Locate every uninfected red blood cell.
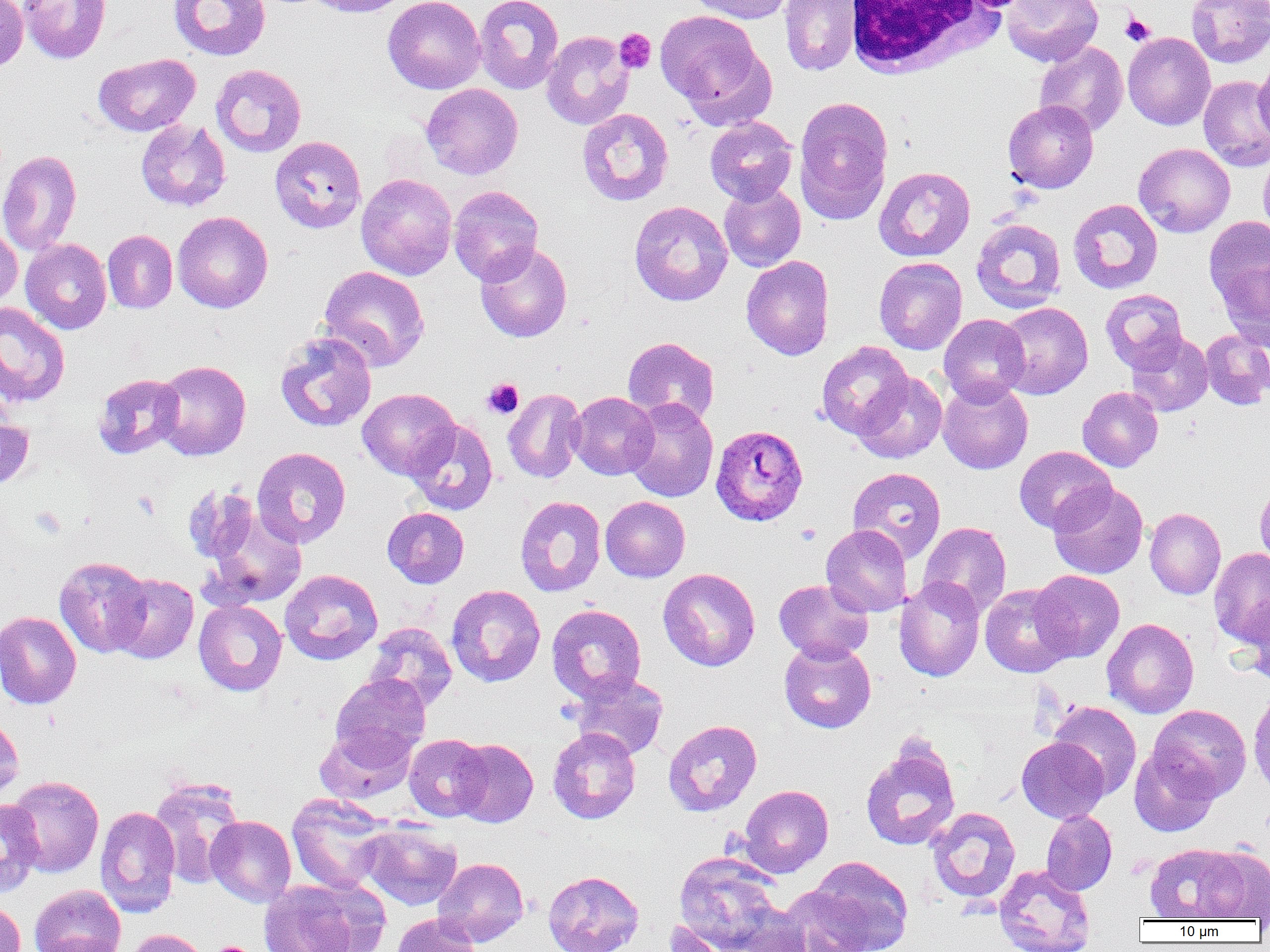
Approximate bounding boxes as named x1/y1/x2/y2 corners in pixels.
Uninfected red blood cells: (x1=0, y1=0, x2=28, y2=73), (x1=20, y1=0, x2=111, y2=64), (x1=168, y1=0, x2=270, y2=60), (x1=304, y1=0, x2=414, y2=17), (x1=383, y1=0, x2=485, y2=94), (x1=474, y1=0, x2=564, y2=94), (x1=685, y1=0, x2=794, y2=24), (x1=1002, y1=0, x2=1103, y2=67), (x1=1186, y1=0, x2=1270, y2=68), (x1=779, y1=1, x2=860, y2=76), (x1=654, y1=9, x2=769, y2=117), (x1=541, y1=31, x2=634, y2=129), (x1=1123, y1=32, x2=1215, y2=130), (x1=1034, y1=42, x2=1128, y2=136), (x1=93, y1=54, x2=201, y2=136), (x1=1254, y1=57, x2=1270, y2=142), (x1=210, y1=64, x2=307, y2=157), (x1=1199, y1=76, x2=1270, y2=172), (x1=420, y1=83, x2=523, y2=179), (x1=793, y1=96, x2=894, y2=225), (x1=1002, y1=100, x2=1099, y2=194), (x1=577, y1=108, x2=674, y2=206), (x1=705, y1=116, x2=798, y2=205), (x1=136, y1=119, x2=231, y2=211), (x1=269, y1=136, x2=366, y2=234), (x1=1134, y1=143, x2=1235, y2=237), (x1=0, y1=149, x2=82, y2=257), (x1=1258, y1=150, x2=1270, y2=242), (x1=874, y1=167, x2=975, y2=261), (x1=356, y1=173, x2=457, y2=280), (x1=719, y1=181, x2=806, y2=272), (x1=448, y1=185, x2=543, y2=284), (x1=1068, y1=199, x2=1163, y2=293), (x1=629, y1=200, x2=733, y2=306), (x1=172, y1=211, x2=273, y2=313), (x1=1204, y1=215, x2=1270, y2=309), (x1=971, y1=218, x2=1066, y2=313), (x1=0, y1=222, x2=22, y2=309), (x1=102, y1=230, x2=177, y2=313), (x1=21, y1=238, x2=111, y2=334), (x1=474, y1=242, x2=572, y2=342), (x1=741, y1=255, x2=834, y2=361), (x1=874, y1=257, x2=967, y2=355), (x1=1218, y1=258, x2=1270, y2=348), (x1=319, y1=265, x2=430, y2=371), (x1=1100, y1=289, x2=1188, y2=373), (x1=996, y1=301, x2=1093, y2=398), (x1=0, y1=302, x2=70, y2=407), (x1=939, y1=314, x2=1030, y2=406), (x1=1201, y1=328, x2=1270, y2=410), (x1=274, y1=330, x2=377, y2=432), (x1=1126, y1=331, x2=1213, y2=416), (x1=622, y1=336, x2=719, y2=426), (x1=816, y1=341, x2=913, y2=439), (x1=154, y1=360, x2=251, y2=460), (x1=853, y1=371, x2=947, y2=463), (x1=92, y1=373, x2=184, y2=459), (x1=938, y1=379, x2=1033, y2=474), (x1=1077, y1=386, x2=1163, y2=472), (x1=357, y1=388, x2=459, y2=480), (x1=503, y1=388, x2=586, y2=483), (x1=568, y1=392, x2=658, y2=480), (x1=623, y1=397, x2=718, y2=502), (x1=0, y1=414, x2=34, y2=489), (x1=405, y1=419, x2=498, y2=515), (x1=1014, y1=446, x2=1115, y2=534), (x1=252, y1=447, x2=351, y2=548), (x1=847, y1=467, x2=946, y2=563), (x1=1255, y1=481, x2=1270, y2=571), (x1=1048, y1=483, x2=1148, y2=579), (x1=182, y1=484, x2=259, y2=565), (x1=515, y1=495, x2=606, y2=597), (x1=600, y1=496, x2=690, y2=582), (x1=382, y1=507, x2=469, y2=588), (x1=1145, y1=508, x2=1226, y2=599), (x1=205, y1=510, x2=307, y2=609), (x1=919, y1=521, x2=1011, y2=618), (x1=821, y1=524, x2=912, y2=617), (x1=1209, y1=547, x2=1270, y2=647), (x1=54, y1=556, x2=152, y2=657), (x1=658, y1=568, x2=760, y2=671), (x1=280, y1=569, x2=383, y2=665), (x1=1030, y1=570, x2=1124, y2=662), (x1=110, y1=573, x2=199, y2=664), (x1=894, y1=577, x2=985, y2=681), (x1=774, y1=579, x2=873, y2=663), (x1=980, y1=584, x2=1074, y2=678), (x1=446, y1=585, x2=546, y2=687), (x1=1240, y1=594, x2=1269, y2=684), (x1=194, y1=600, x2=287, y2=696), (x1=546, y1=604, x2=646, y2=703), (x1=0, y1=611, x2=81, y2=709), (x1=1102, y1=618, x2=1199, y2=718), (x1=365, y1=622, x2=457, y2=711), (x1=779, y1=639, x2=876, y2=734), (x1=569, y1=672, x2=669, y2=760), (x1=330, y1=673, x2=430, y2=765), (x1=1249, y1=688, x2=1270, y2=797), (x1=1048, y1=701, x2=1142, y2=799), (x1=1148, y1=704, x2=1252, y2=801), (x1=0, y1=715, x2=24, y2=804), (x1=663, y1=719, x2=762, y2=816), (x1=314, y1=726, x2=415, y2=804), (x1=548, y1=727, x2=641, y2=824), (x1=404, y1=734, x2=490, y2=821), (x1=1016, y1=736, x2=1109, y2=823), (x1=450, y1=738, x2=538, y2=828), (x1=860, y1=741, x2=961, y2=850), (x1=1129, y1=745, x2=1219, y2=837), (x1=6, y1=776, x2=104, y2=877), (x1=148, y1=777, x2=246, y2=888), (x1=739, y1=784, x2=833, y2=877), (x1=287, y1=794, x2=393, y2=893), (x1=0, y1=799, x2=43, y2=897), (x1=95, y1=806, x2=181, y2=917), (x1=927, y1=807, x2=1020, y2=903), (x1=1041, y1=809, x2=1117, y2=895), (x1=206, y1=815, x2=296, y2=907), (x1=359, y1=821, x2=462, y2=911), (x1=1145, y1=843, x2=1243, y2=921), (x1=1194, y1=846, x2=1270, y2=920), (x1=674, y1=852, x2=783, y2=951), (x1=805, y1=856, x2=914, y2=951), (x1=433, y1=857, x2=529, y2=947), (x1=994, y1=864, x2=1096, y2=951), (x1=543, y1=870, x2=644, y2=952), (x1=258, y1=879, x2=373, y2=952), (x1=28, y1=884, x2=126, y2=952), (x1=776, y1=884, x2=874, y2=952), (x1=0, y1=899, x2=26, y2=952), (x1=729, y1=902, x2=813, y2=952), (x1=391, y1=913, x2=482, y2=952), (x1=664, y1=920, x2=739, y2=952), (x1=125, y1=928, x2=208, y2=952), (x1=38, y1=934, x2=127, y2=952).

slide_level_diagnosis: Plasmodium ovale
preparation: thin blood smear
modality: light microscopy
plasmodium_ovale_infected_red_blood_cell_locations: 'approximate bounding boxes as named x1/y1/x2/y2 corners in pixels: (x1=711, y1=425, x2=808, y2=526)'
white_blood_cell_locations: 'approximate bounding boxes as named x1/y1/x2/y2 corners in pixels: (x1=845, y1=0, x2=1009, y2=80)'
field_of_view: single
image_size: 1270×952 pixels
magnification: 1000x
platelet_locations: 'approximate bounding boxes as named x1/y1/x2/y2 corners in pixels: (x1=1120, y1=13, x2=1154, y2=46), (x1=614, y1=28, x2=655, y2=74), (x1=482, y1=378, x2=524, y2=419), (x1=132, y1=491, x2=160, y2=519), (x1=31, y1=507, x2=66, y2=539), (x1=796, y1=523, x2=821, y2=545), (x1=210, y1=942, x2=255, y2=952)'